Point out each malaria parasite.
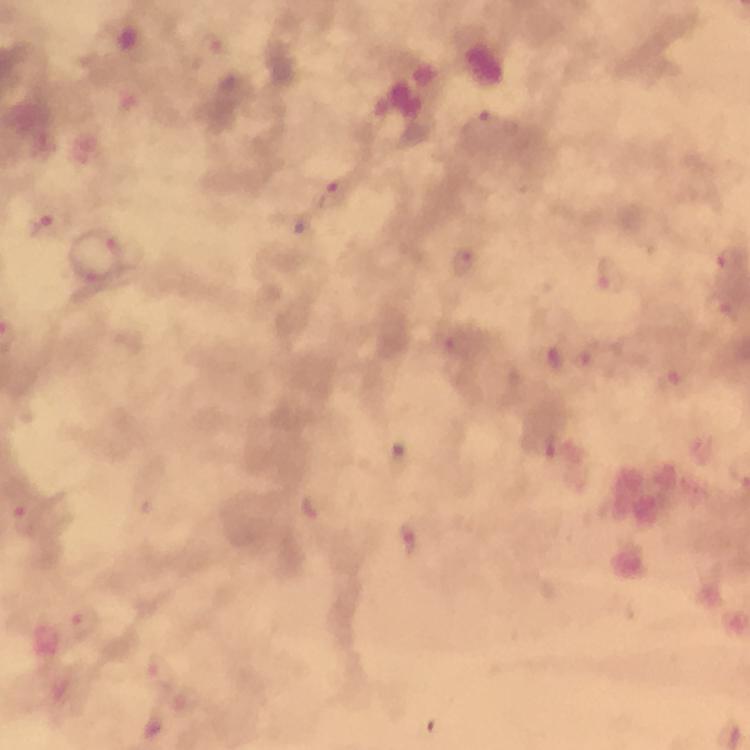

Approximate centers as {x, y} in pixels.
Malaria parasites: {331, 194}, {45, 222}, {121, 246}, {462, 262}, {611, 276}, {93, 282}, {720, 305}, {552, 358}, {671, 382}, {546, 446}, {26, 519}, {409, 539}, {84, 623}, {156, 672}.

Photographed through the microscope with a smartphone camera. Giemsa stain. A crop from one field of view. From a malaria diagnostic workup. 100x magnification. Thick smear. Image is 750×750 pixels. Immersion oil was used.